Draw a bounding box around every leukocyte (white blood cell).
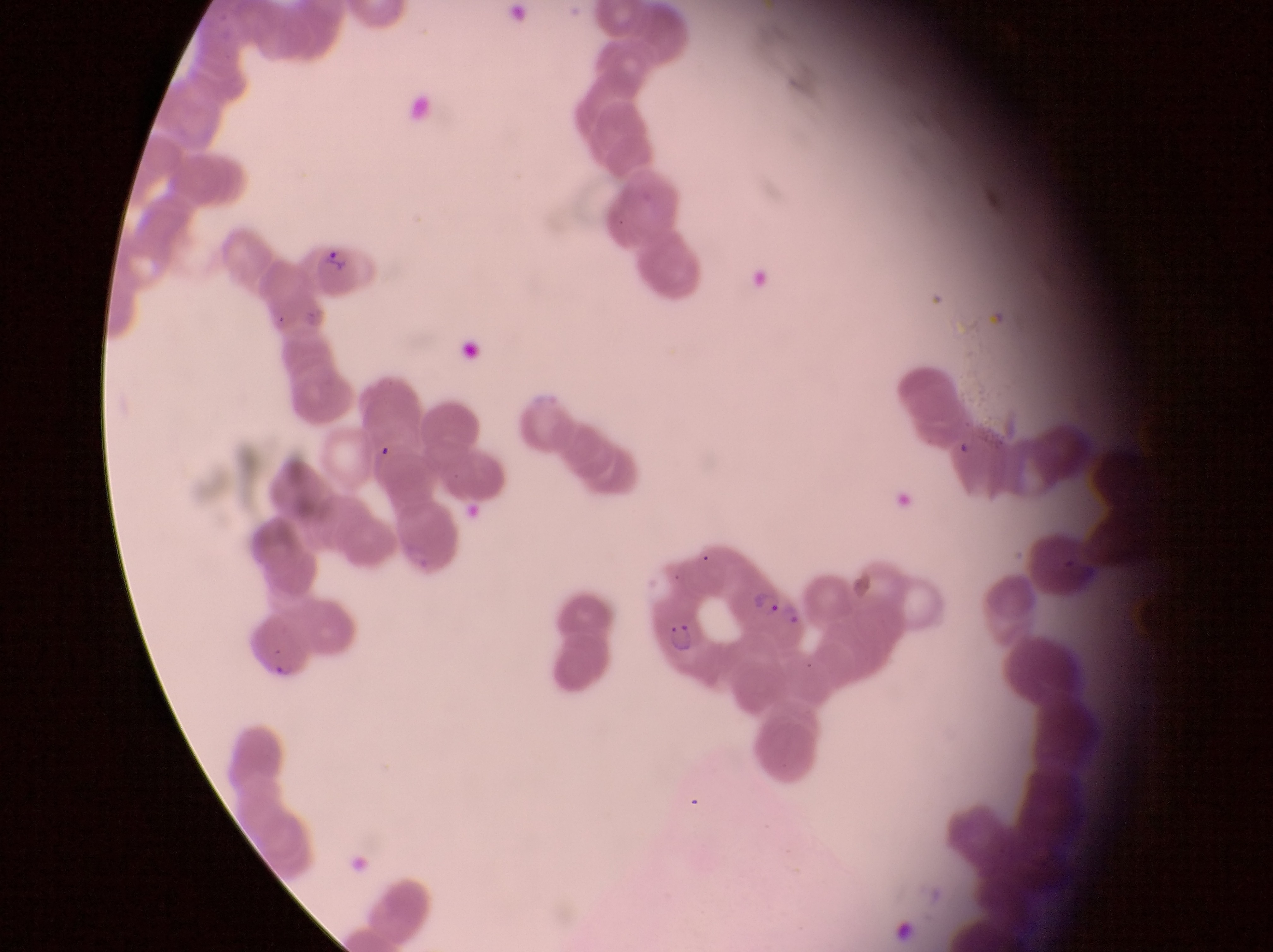

No leukocytes observed.

image_size: 1273×952 pixels
capture: smartphone photograph through the eyepiece of an Olympus CX-23 microscope
field_of_view: single
country: Uganda
magnification: 1000x
parasitised_red_blood_cell_locations: 'approximate bounding boxes as [left, top, right, bottom] in pixels: [309, 234, 364, 302], [734, 565, 808, 645], [652, 605, 715, 670]'
preparation: thin blood smear